Name the cell type shown.
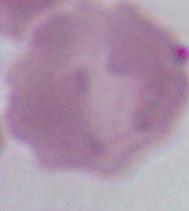
An erythrocyte.

modality = micrograph
magnification = 1000x